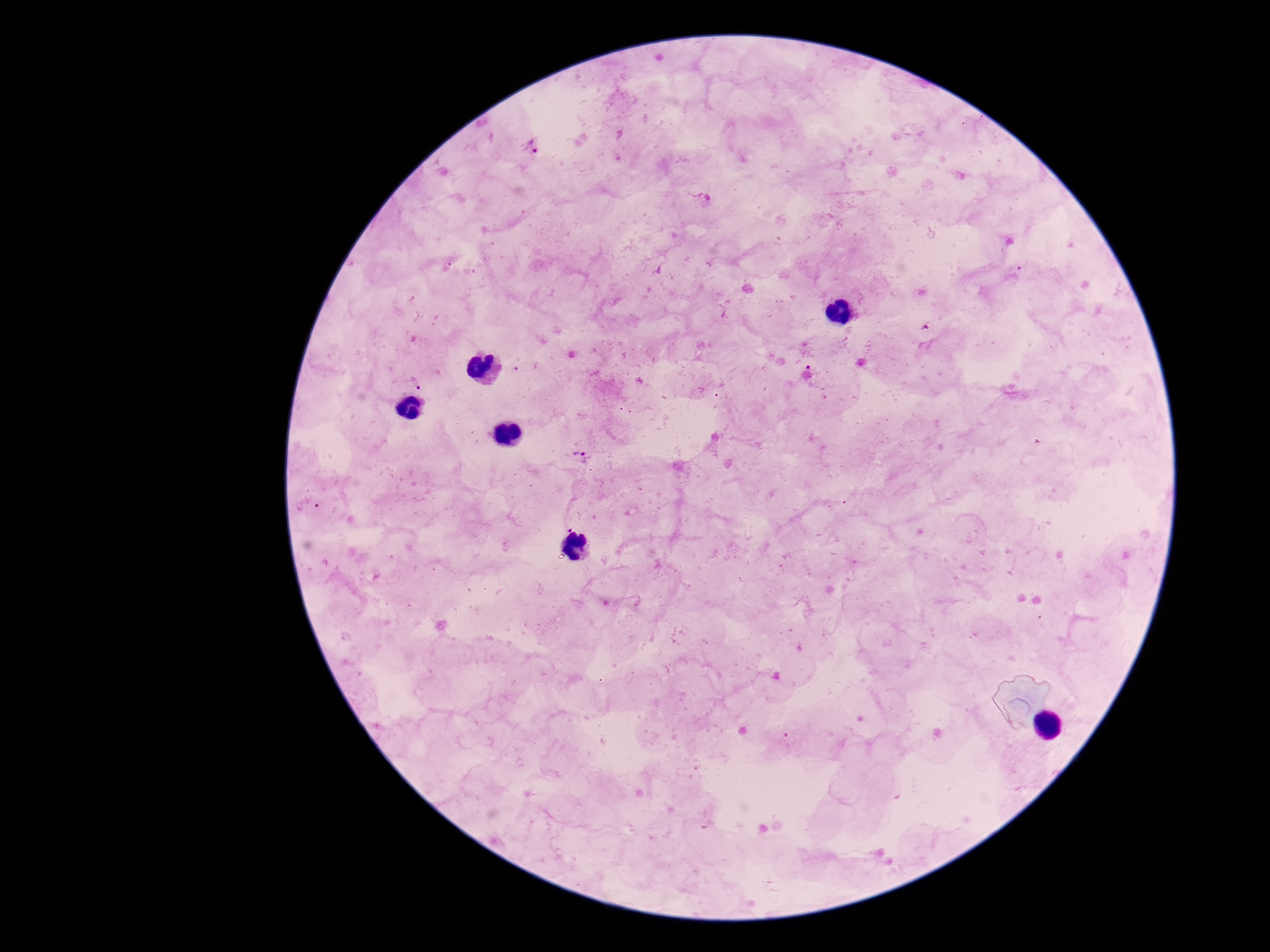
{
  "stain": "Giemsa",
  "field_of_view": "one from this slide",
  "patient_malaria_status": "positive",
  "preparation": "thick peripheral-blood smear",
  "image_size": "1270×952 pixels",
  "capture": "smartphone camera through the microscope eyepiece",
  "magnification": "100x",
  "plasmodium_parasite_locations": "approximate centers as {x, y} in pixels: {533, 147}, {414, 383}, {578, 456}"
}